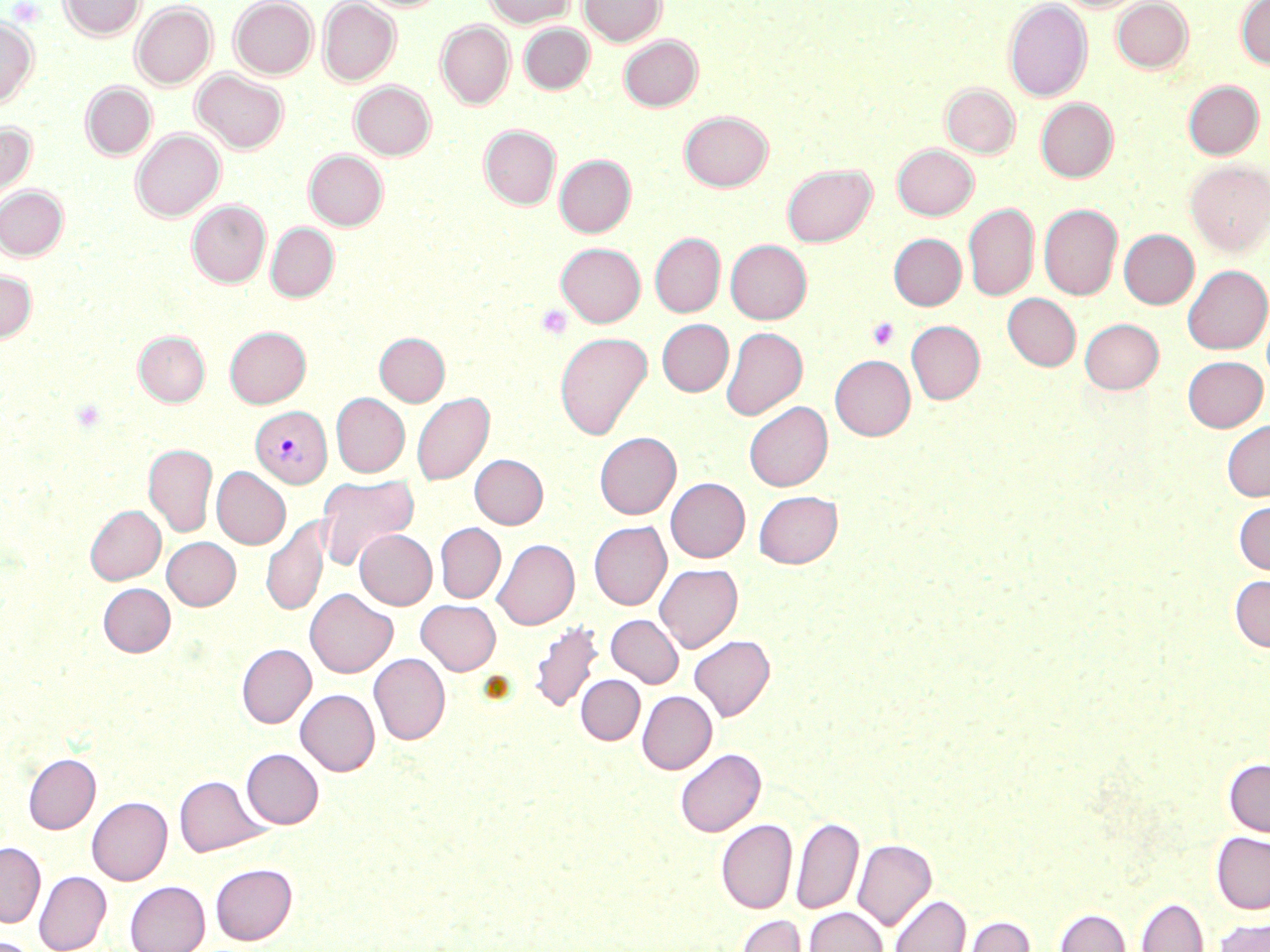

slide-level diagnosis = Plasmodium vivax
preparation = thin blood smear
image size = 1270×952 pixels
magnification = 1000x
platelet locations = approximate bounding boxes as (x1,y1)-(x2,y2) corner pairs in pixels: (7,1)-(45,27), (536,304)-(572,340), (867,317)-(900,350)
field of view = single
uninfected red blood cell locations = approximate bounding boxes as (x1,y1)-(x2,y2) corner pairs in pixels: (59,0)-(145,39), (229,0)-(317,79), (318,0)-(401,86), (484,0)-(575,28), (580,0)-(666,46), (1004,1)-(1092,101), (1111,1)-(1193,73), (1235,1)-(1270,68), (131,2)-(216,89), (132,2)-(316,86), (0,17)-(37,108), (437,21)-(514,109), (520,23)-(594,94), (618,35)-(703,111), (192,70)-(288,153), (1183,80)-(1264,159), (350,81)-(435,160), (81,82)-(156,159), (941,82)-(1020,158), (1036,98)-(1118,182), (679,111)-(773,191), (0,121)-(36,207), (480,125)-(561,209), (131,129)-(225,221), (892,144)-(979,220), (305,150)-(387,230), (555,155)-(636,237), (1185,160)-(1270,256), (782,164)-(876,247), (0,186)-(68,261), (187,201)-(270,288), (963,203)-(1038,301), (1039,203)-(1123,300), (266,223)-(338,302), (1119,229)-(1198,308), (650,233)-(725,317), (889,233)-(966,310), (726,240)-(812,324), (556,242)-(645,327), (1183,265)-(1269,354), (0,271)-(37,343), (1003,294)-(1081,371), (1080,318)-(1164,394), (657,319)-(733,396), (906,321)-(985,404), (225,326)-(311,408), (721,327)-(807,420), (134,331)-(209,406), (555,332)-(652,440), (375,333)-(449,406), (830,355)-(916,440), (1182,355)-(1268,432), (412,392)-(494,485), (331,393)-(409,477), (744,401)-(832,491), (1222,420)-(1270,501), (595,432)-(681,519), (144,444)-(217,536), (470,454)-(548,529), (212,467)-(290,549), (316,473)-(419,570), (666,477)-(750,562), (753,490)-(842,568), (1234,500)-(1270,575), (85,505)-(165,584), (260,516)-(329,616), (589,521)-(671,610), (435,523)-(505,602), (355,529)-(437,610), (162,537)-(241,610), (492,539)-(579,629), (655,563)-(742,652), (1230,575)-(1270,652), (98,583)-(175,656), (305,588)-(397,677), (416,600)-(501,674), (606,614)-(683,687), (529,621)-(604,715), (689,635)-(775,720), (237,644)-(316,728), (369,653)-(450,744), (576,675)-(645,744), (296,689)-(380,776), (637,691)-(717,774), (241,748)-(323,828), (675,748)-(765,836), (24,753)-(100,833), (1224,758)-(1270,837), (175,775)-(269,856), (87,796)-(172,885), (791,816)-(863,914), (716,819)-(797,913), (1212,832)-(1270,913), (852,839)-(936,931), (0,842)-(45,927), (210,862)-(297,944), (34,871)-(111,952), (125,880)-(210,952), (889,894)-(971,952), (1135,898)-(1208,952), (804,907)-(887,952), (1054,909)-(1130,952), (733,914)-(809,952), (961,915)-(1035,952), (1212,917)-(1270,952), (1,937)-(39,952)
modality = optical microscopy
Plasmodium vivax-infected red blood cell locations = approximate bounding boxes as (x1,y1)-(x2,y2) corner pairs in pixels: (250,406)-(332,488)
stain = May-Grünwald-Giemsa